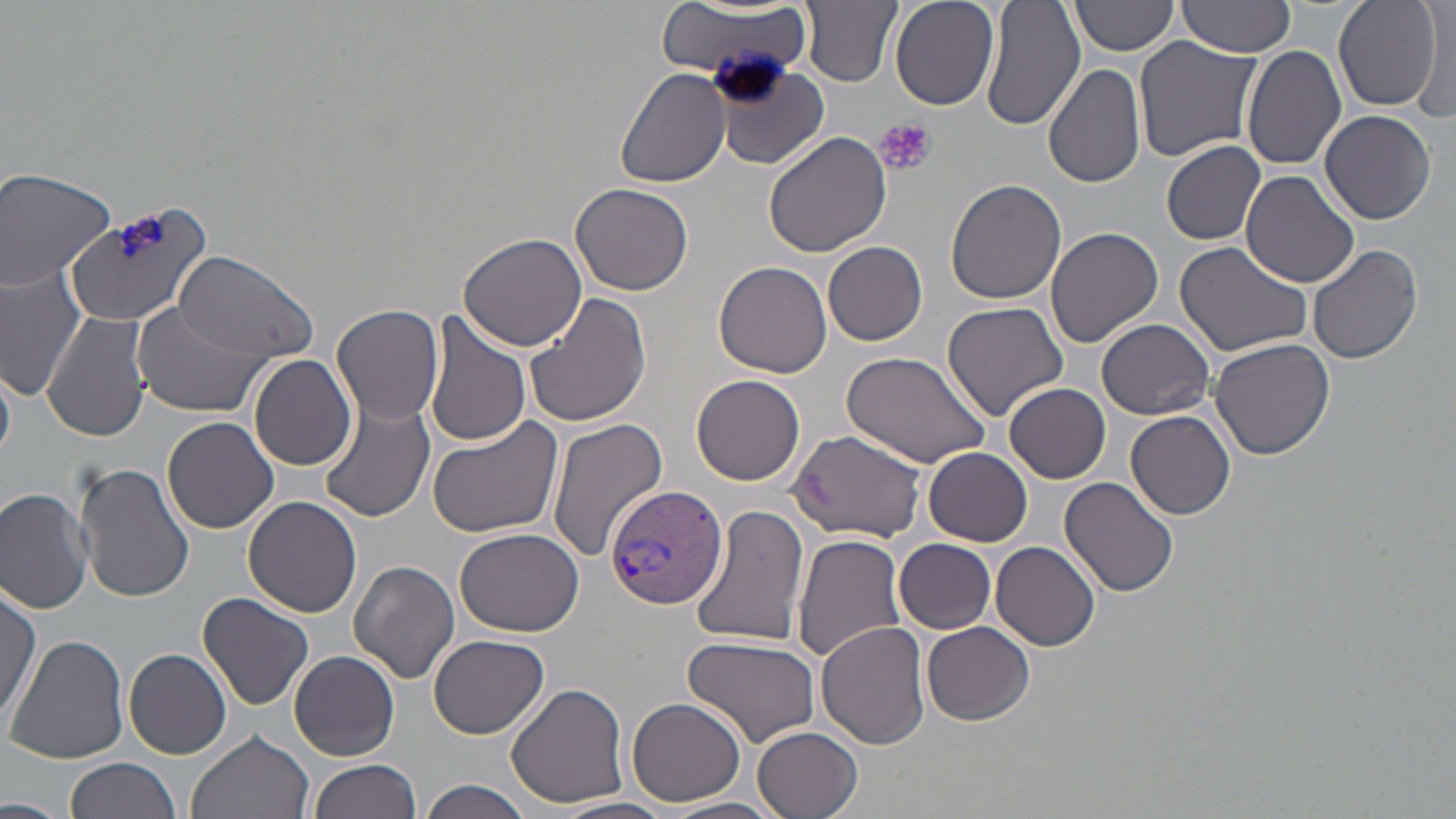
slide-level diagnosis = Plasmodium vivax
uninfected red blood cell locations = approximate bounding boxes as named x1/y1/x2/y2 corners in pixels: (x1=802, y1=0, x2=901, y2=87), (x1=890, y1=0, x2=1000, y2=110), (x1=982, y1=0, x2=1085, y2=131), (x1=1072, y1=0, x2=1179, y2=57), (x1=1178, y1=0, x2=1298, y2=57), (x1=1333, y1=1, x2=1441, y2=110), (x1=657, y1=2, x2=812, y2=88), (x1=1411, y1=6, x2=1454, y2=122), (x1=1133, y1=35, x2=1262, y2=163), (x1=1244, y1=45, x2=1347, y2=170), (x1=1062, y1=56, x2=1234, y2=182), (x1=710, y1=59, x2=831, y2=168), (x1=1043, y1=63, x2=1147, y2=189), (x1=616, y1=66, x2=732, y2=187), (x1=1320, y1=109, x2=1437, y2=224), (x1=762, y1=132, x2=892, y2=260), (x1=1161, y1=138, x2=1266, y2=244), (x1=0, y1=166, x2=119, y2=292), (x1=1242, y1=170, x2=1360, y2=290), (x1=946, y1=177, x2=1067, y2=304), (x1=570, y1=182, x2=693, y2=295), (x1=62, y1=200, x2=221, y2=328), (x1=1045, y1=226, x2=1164, y2=348), (x1=458, y1=231, x2=586, y2=353), (x1=1175, y1=240, x2=1315, y2=358), (x1=822, y1=241, x2=928, y2=346), (x1=1307, y1=244, x2=1423, y2=366), (x1=173, y1=251, x2=319, y2=366), (x1=714, y1=261, x2=833, y2=379), (x1=0, y1=264, x2=87, y2=401), (x1=525, y1=290, x2=653, y2=427), (x1=133, y1=300, x2=261, y2=418), (x1=942, y1=301, x2=1068, y2=419), (x1=333, y1=306, x2=443, y2=426), (x1=43, y1=311, x2=151, y2=443), (x1=421, y1=312, x2=532, y2=449), (x1=1097, y1=318, x2=1215, y2=419), (x1=1208, y1=337, x2=1336, y2=461), (x1=839, y1=348, x2=994, y2=469), (x1=250, y1=354, x2=356, y2=471), (x1=692, y1=375, x2=805, y2=486), (x1=1005, y1=384, x2=1111, y2=484), (x1=179, y1=389, x2=328, y2=516), (x1=321, y1=400, x2=436, y2=522), (x1=1126, y1=411, x2=1236, y2=520), (x1=162, y1=417, x2=280, y2=535), (x1=427, y1=417, x2=565, y2=541), (x1=547, y1=419, x2=670, y2=563), (x1=788, y1=429, x2=929, y2=540), (x1=923, y1=446, x2=1034, y2=545), (x1=75, y1=461, x2=195, y2=602), (x1=1060, y1=478, x2=1179, y2=599), (x1=0, y1=485, x2=95, y2=614), (x1=243, y1=495, x2=362, y2=618), (x1=692, y1=504, x2=808, y2=650), (x1=454, y1=527, x2=581, y2=636), (x1=792, y1=534, x2=907, y2=664), (x1=895, y1=538, x2=995, y2=633), (x1=992, y1=541, x2=1100, y2=653), (x1=349, y1=560, x2=460, y2=684), (x1=0, y1=584, x2=41, y2=730), (x1=198, y1=593, x2=314, y2=711), (x1=922, y1=620, x2=1035, y2=725), (x1=817, y1=621, x2=931, y2=749), (x1=8, y1=634, x2=129, y2=766), (x1=429, y1=634, x2=548, y2=738), (x1=682, y1=635, x2=821, y2=748), (x1=124, y1=647, x2=232, y2=759), (x1=290, y1=651, x2=400, y2=760), (x1=506, y1=683, x2=632, y2=808), (x1=627, y1=696, x2=746, y2=805), (x1=751, y1=725, x2=865, y2=818), (x1=186, y1=729, x2=315, y2=819), (x1=65, y1=759, x2=180, y2=819), (x1=308, y1=759, x2=421, y2=819), (x1=420, y1=778, x2=536, y2=819), (x1=0, y1=795, x2=67, y2=818), (x1=552, y1=797, x2=676, y2=819), (x1=662, y1=798, x2=786, y2=819)
magnification = 1000x
preparation = thin blood film
platelet locations = approximate bounding boxes as named x1/y1/x2/y2 corners in pixels: (x1=877, y1=117, x2=935, y2=178), (x1=115, y1=215, x2=166, y2=260)
Plasmodium vivax-infected red blood cell locations = approximate bounding boxes as named x1/y1/x2/y2 corners in pixels: (x1=605, y1=484, x2=727, y2=610)
modality = light microscopy
stain = May-Grünwald-Giemsa
image size = 1456×819 pixels
field of view = one of a larger specimen